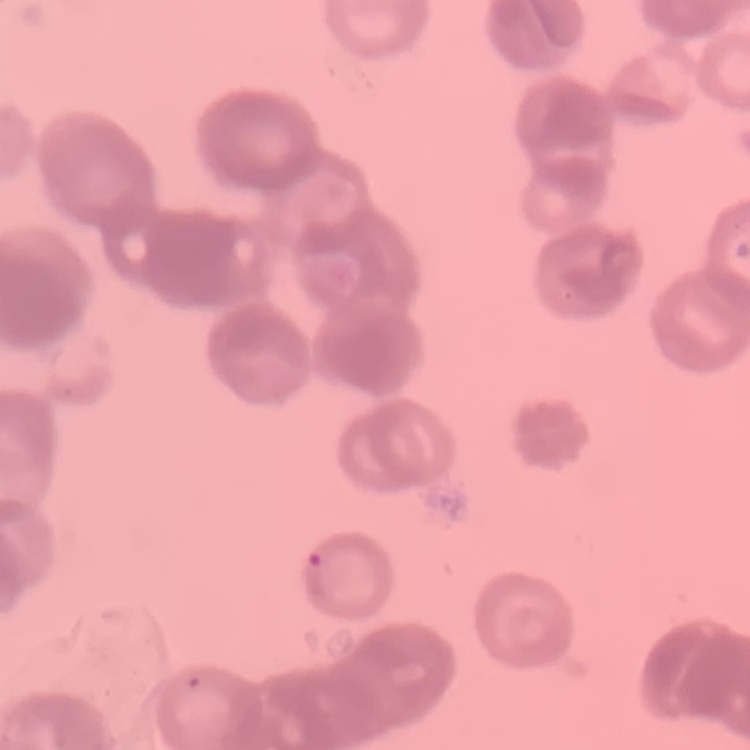
{
  "red_blood_cell_morphology": "rouleaux formation",
  "image_type": "one tile cut from a larger photomicrograph",
  "stain": "Field's or Giemsa",
  "preparation": "thin peripheral smear"
}